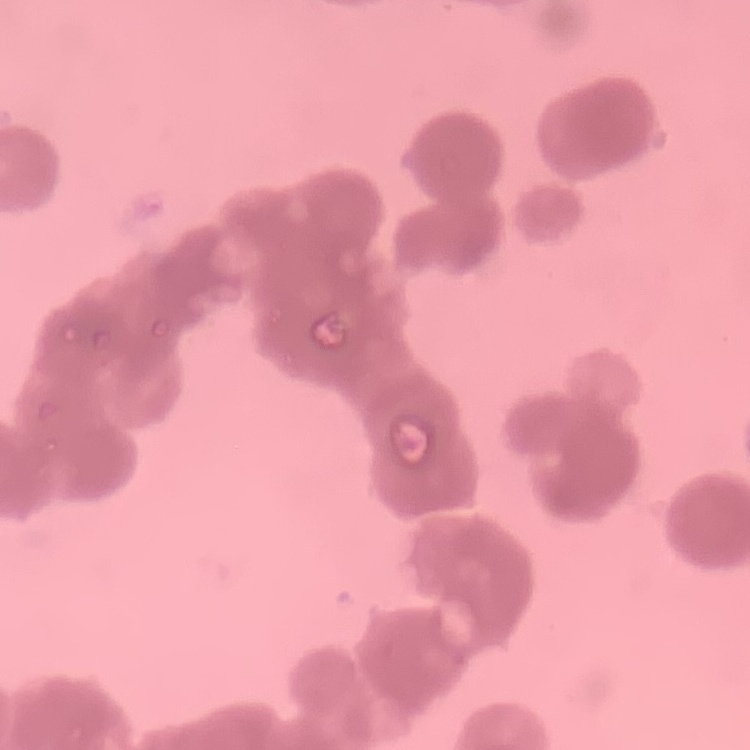

The red blood cells show rouleaux formation. One tile cut from a larger photomicrograph. Thin peripheral smear. Field's or Giemsa stain.